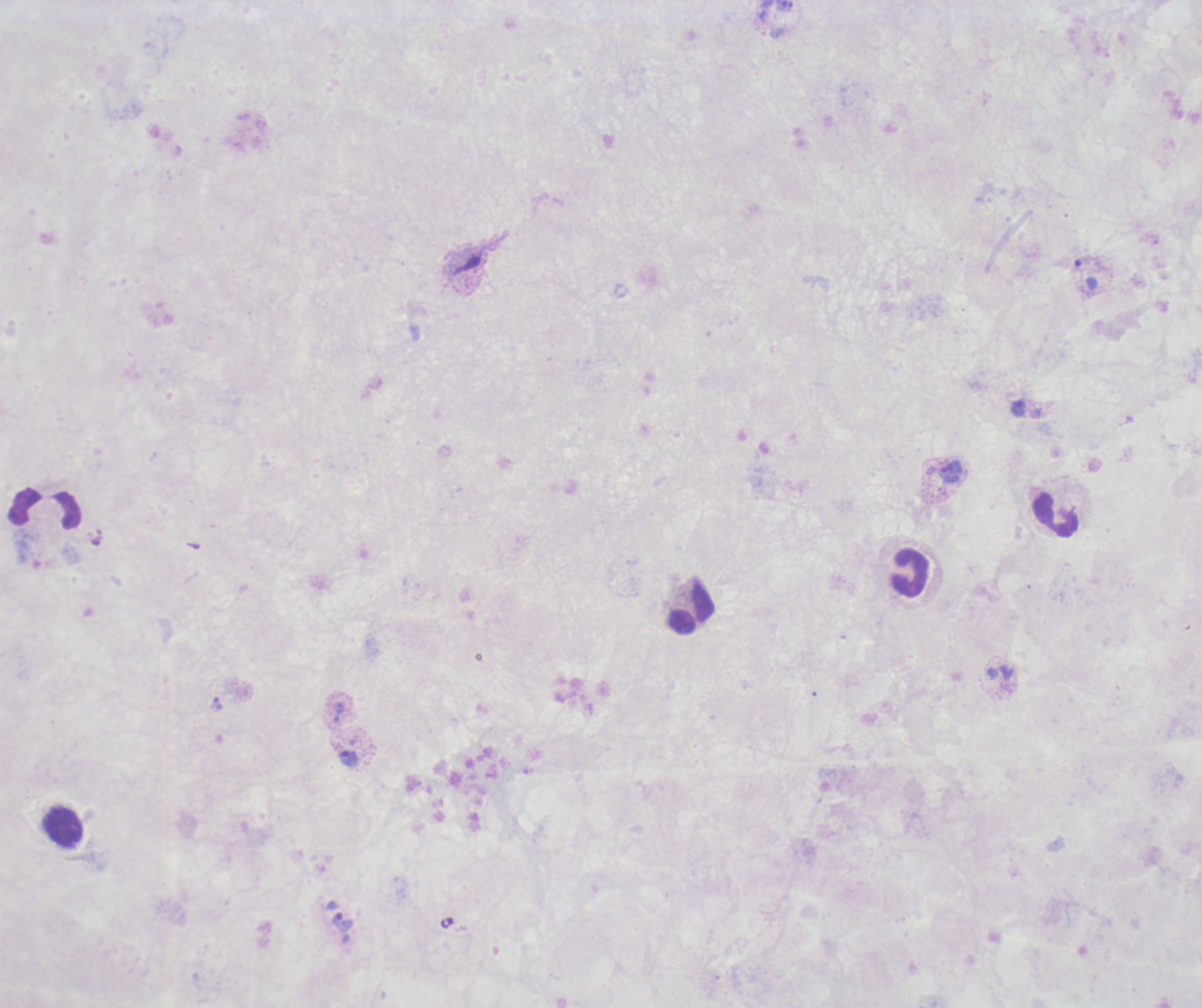
Approximate centers as (x, y) in pixels.
Summary:
  - Leukocyte locations: (45, 508), (1056, 516), (909, 573), (689, 608), (64, 827)
  - Trophozoite locations: (1086, 275), (1018, 407), (951, 471), (1006, 672), (216, 704), (339, 709), (348, 759), (342, 922)
  - Coloration quality: bad
  - Background quality: unsatisfactory
  - Image size: 1202×1008 pixels
  - Context: previously used in a real diagnosis
  - Magnification: 100x
  - Stain: Romanowsky
  - Preparation: thick blood film
  - Result: Plasmodium parasites detected
  - Field of view: single